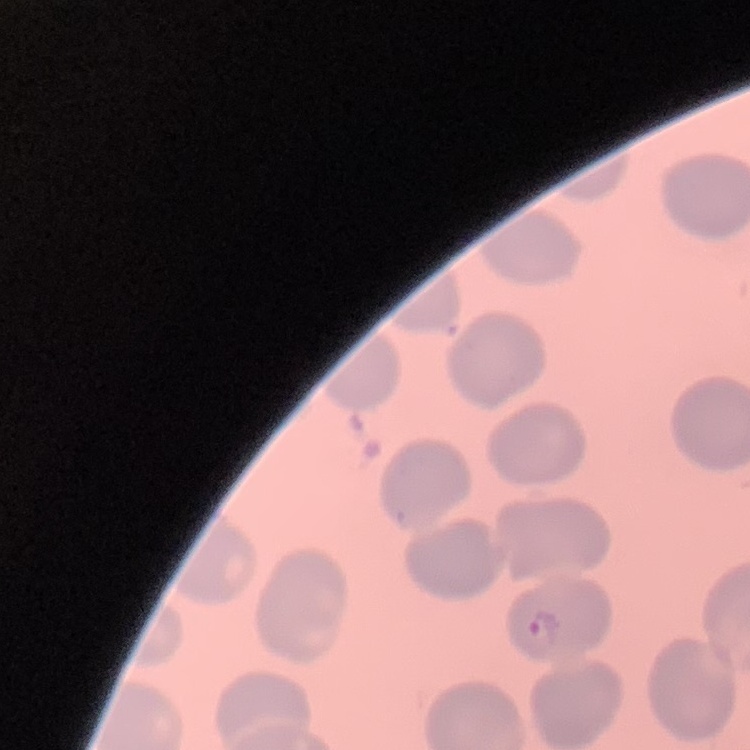

Summary:
  - Red blood cell morphology: no rouleaux formation
  - Image type: one tile cut from a larger photomicrograph
  - Preparation: thin blood film
  - Stain: Field's or Giemsa